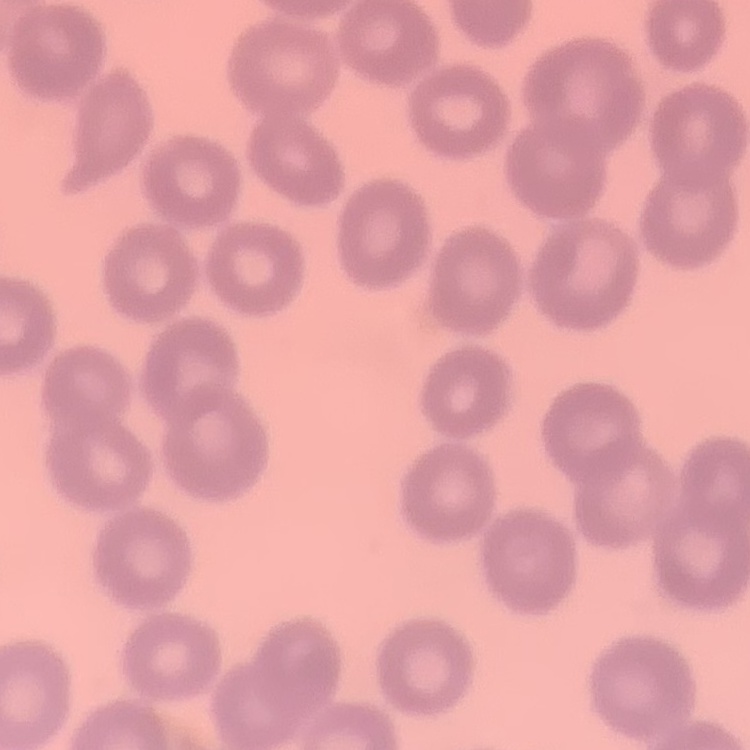

Summary:
  - Red blood cell morphology: no rouleaux formation
  - Image type: one tile cut from a larger photomicrograph
  - Stain: Field's or Giemsa
  - Preparation: thin peripheral smear